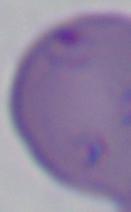

Photomicrograph. A Babesia parasite is shown. 1000x magnification.